Locate every Plasmodium malariae-infected red blood cell.
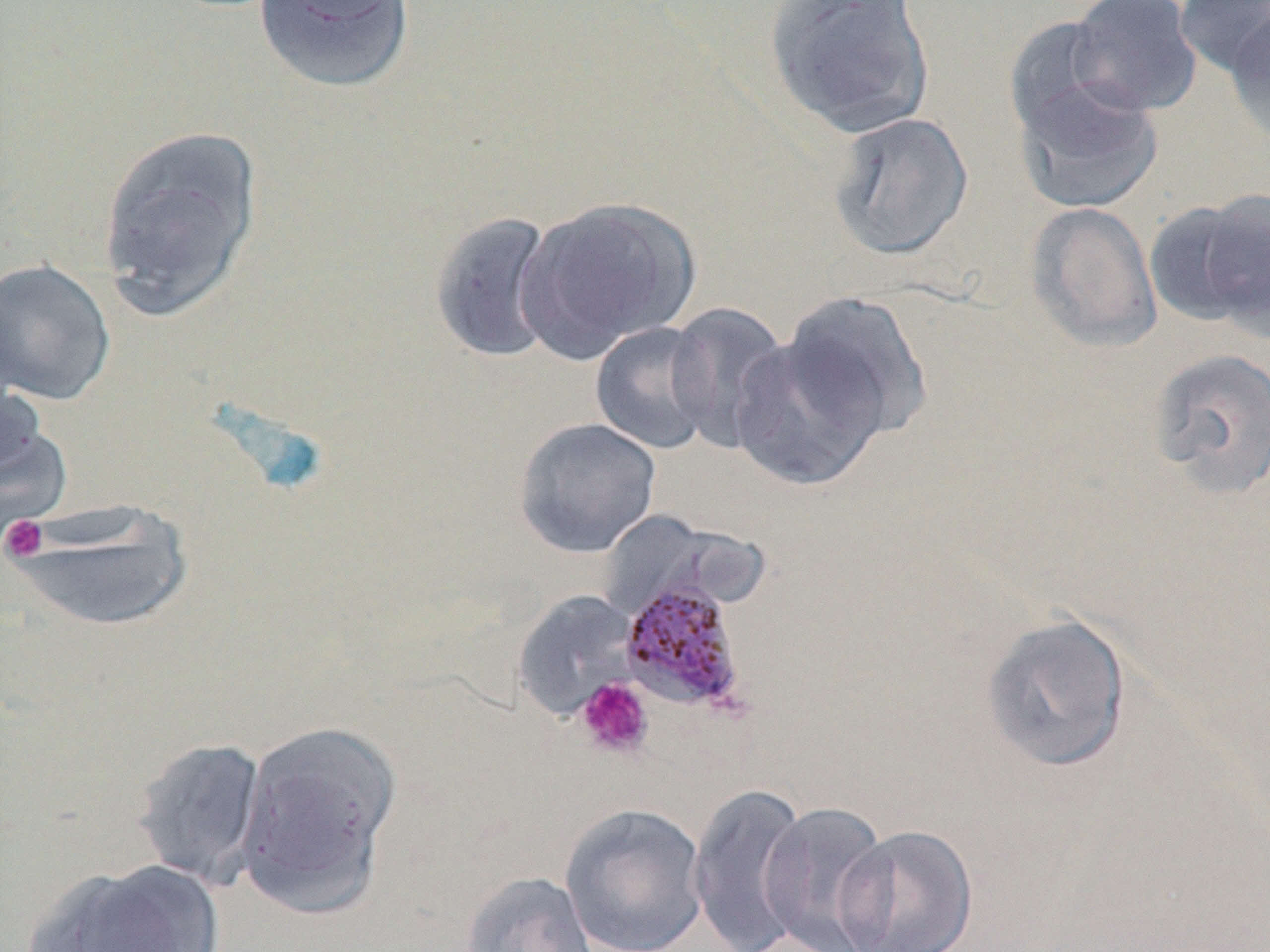
Approximate bounding boxes as (x1,y1)-(x2,y2) corner pairs in pixels.
Plasmodium malariae-infected red blood cells: (616,570)-(753,720).

Platelet locations: (1,515)-(49,562), (574,677)-(655,760). Uninfected red blood cell locations: (762,0)-(937,140), (1065,0)-(1204,117), (1173,0)-(1270,79), (253,1)-(416,96), (1222,11)-(1270,145), (1003,15)-(1125,138), (1012,73)-(1164,215), (825,110)-(976,261), (96,125)-(263,321), (514,195)-(702,364), (1144,196)-(1265,328), (1025,201)-(1162,353), (428,210)-(562,364), (0,258)-(117,406), (778,291)-(935,445), (664,303)-(792,453), (589,321)-(718,455), (730,333)-(887,492), (1146,347)-(1270,500), (0,403)-(72,550), (513,417)-(662,559), (5,498)-(197,633), (512,590)-(640,721), (980,613)-(1132,774), (234,719)-(402,914), (131,736)-(269,889), (687,782)-(812,952), (757,801)-(893,952), (559,802)-(709,952), (834,824)-(979,952), (28,858)-(225,952), (459,870)-(600,952). Slide-level diagnosis: Plasmodium malariae. Single field of view. May-Grünwald-Giemsa stain. Optical microscopy. Image is 1270×952 pixels. Thin blood smear. Captured at 1000x magnification.